Give the position of every Plasmodium parasite.
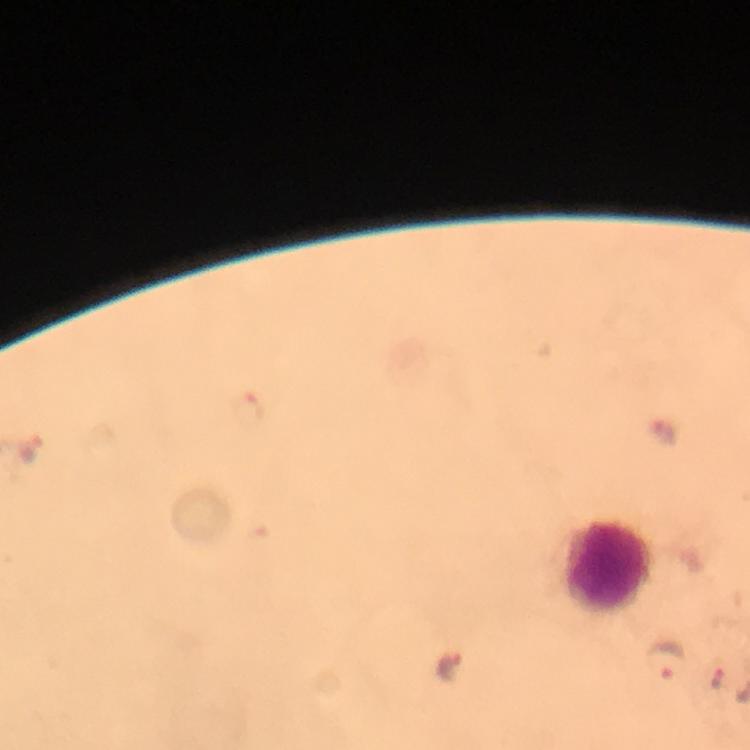
Approximate centers as {x, y} in pixels.
Plasmodium parasites: {32, 451}, {663, 660}, {716, 678}.

Summary:
  - Leukocyte locations: {606, 566}
  - Preparation: thick blood film
  - Immersion oil: used
  - Image size: 750×750 pixels
  - Context: from a diagnostic examination for malaria
  - Stain: Giemsa
  - Magnification: 100x
  - Cropped from: a single field of view
  - Capture: smartphone photograph through a microscope